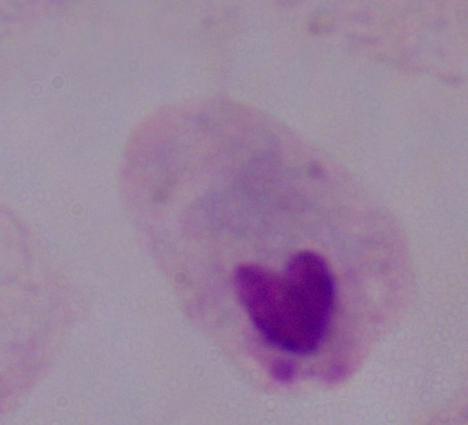

magnification = 1000x
modality = photomicrograph
identification = trichomonad